Classify this cell by malaria status.
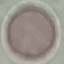
Uninfected.

Thin blood film. Photographed with a smartphone camera at the microscope eyepiece. Giemsa stain. Automatically extracted cell patch, resized to 64 × 64 pixels.